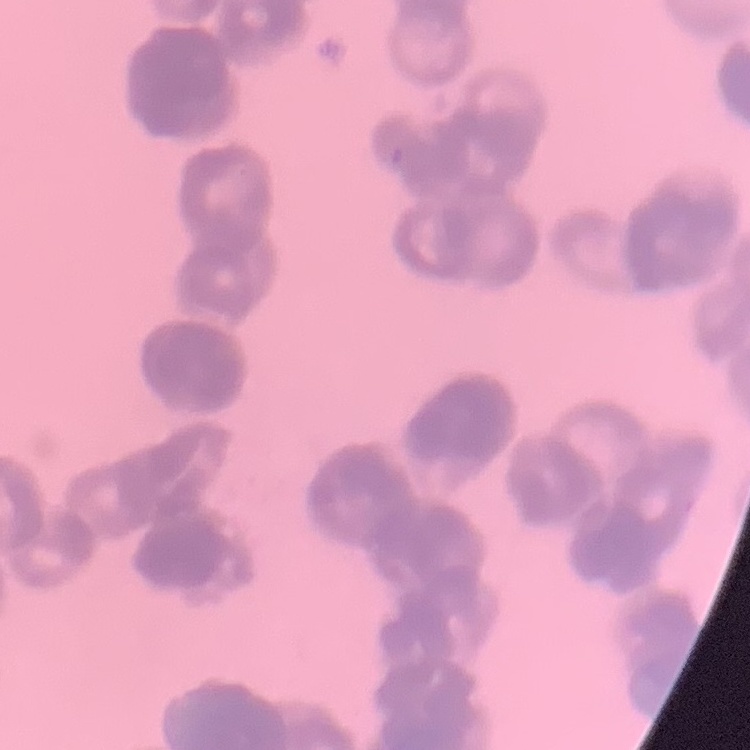

The erythrocytes show rouleaux formation. Thin blood film. Field's or Giemsa stain. One tile cut from a larger photomicrograph.